Name the parasite shown.
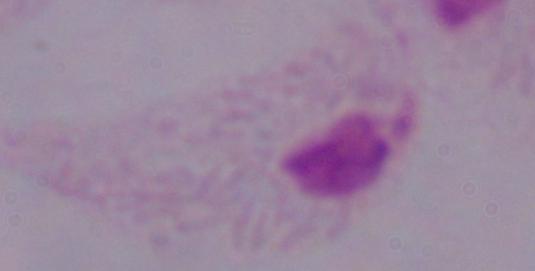
A trichomonad.

Captured at 1000x magnification. Photomicrograph.